Locate every blood parasite and identify its species.
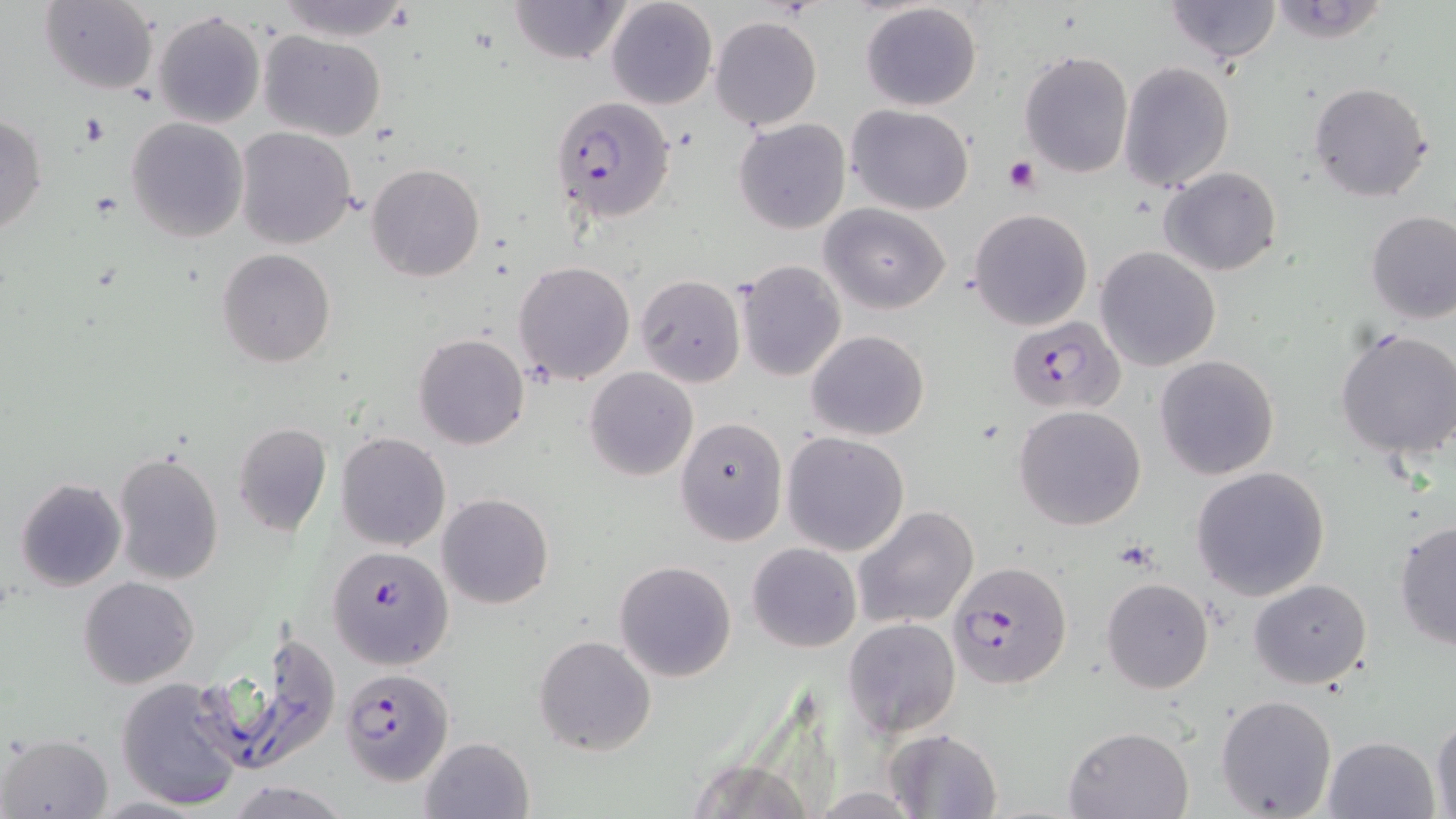
Approximate bounding boxes as (x1, y1, x2, y2) in pixels.
Plasmodium falciparum-infected red blood cells: (550, 95, 675, 223), (1012, 316, 1130, 416), (326, 545, 454, 669), (945, 561, 1072, 690), (340, 668, 454, 785).
No Plasmodium ovale, Plasmodium malariae, Plasmodium vivax, Babesia divergens, or Trypanosoma brucei observed.

Summary:
  - Platelet locations: (1003, 155, 1042, 195)
  - Uninfected red blood cell locations: (269, 0, 417, 40), (509, 0, 629, 65), (605, 0, 718, 110), (1165, 0, 1282, 62), (1267, 1, 1391, 43), (38, 2, 159, 93), (860, 2, 982, 112), (153, 10, 266, 128), (710, 16, 822, 132), (258, 29, 386, 141), (1018, 50, 1134, 179), (1119, 60, 1234, 191), (1307, 81, 1434, 202), (846, 104, 974, 214), (0, 115, 47, 238), (126, 117, 250, 242), (735, 118, 852, 235), (235, 127, 358, 248), (365, 162, 486, 282), (1159, 166, 1281, 277), (820, 203, 950, 314), (969, 207, 1092, 330), (1366, 213, 1456, 325), (1095, 247, 1222, 371), (216, 248, 337, 367), (736, 260, 847, 382), (513, 261, 636, 384), (634, 275, 745, 388), (1334, 328, 1456, 463), (806, 329, 930, 441), (413, 333, 529, 450), (1154, 354, 1279, 479), (585, 367, 698, 481), (1013, 405, 1146, 530), (674, 417, 788, 546), (231, 423, 332, 536), (336, 432, 451, 551), (781, 432, 910, 556), (112, 449, 225, 586), (1190, 466, 1331, 601), (14, 477, 125, 591), (437, 494, 554, 610), (852, 505, 980, 630), (1393, 519, 1456, 650), (747, 541, 861, 653), (614, 560, 739, 683), (80, 577, 198, 688), (1101, 577, 1215, 694), (1249, 578, 1374, 689), (843, 618, 961, 736), (209, 633, 342, 774), (534, 635, 656, 757), (117, 676, 248, 812), (1215, 694, 1338, 818), (1430, 712, 1456, 819), (1063, 726, 1195, 817), (885, 727, 1003, 819), (2, 732, 113, 817), (418, 735, 535, 819), (1322, 735, 1441, 819), (682, 756, 817, 819), (224, 779, 353, 818), (90, 795, 207, 818)
  - Slide-level diagnosis: Plasmodium falciparum
  - Image size: 1456×819 pixels
  - Stain: May-Grünwald-Giemsa
  - Preparation: thin blood smear
  - Field of view: single
  - Modality: light microscopy
  - Magnification: 1000x